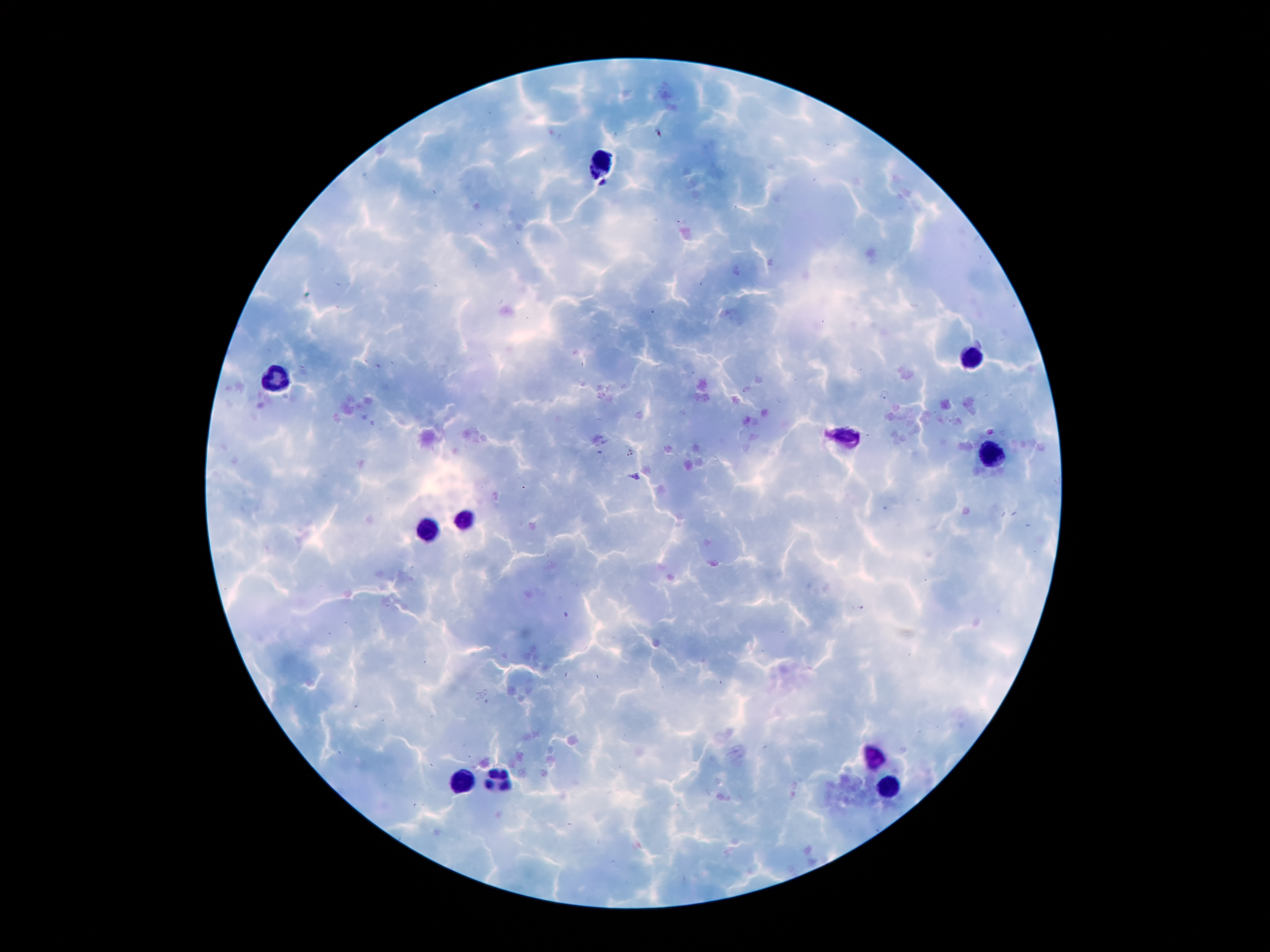

{
  "malaria_parasite_locations": "approximate centers as {x, y} in pixels: {605, 182}",
  "leukocyte_locations": "approximate centers as {x, y} in pixels: {604, 159}, {967, 359}, {277, 379}, {845, 436}, {995, 452}, {463, 520}, {427, 529}, {877, 760}, {468, 781}, {890, 781}, {502, 783}",
  "image_size": "1270×952 pixels",
  "magnification": "100x",
  "capture": "smartphone through the microscope eyepiece",
  "preparation": "thick blood smear",
  "stain": "Giemsa",
  "field_of_view": "single",
  "patient_malaria_status": "infected with Plasmodium falciparum"
}